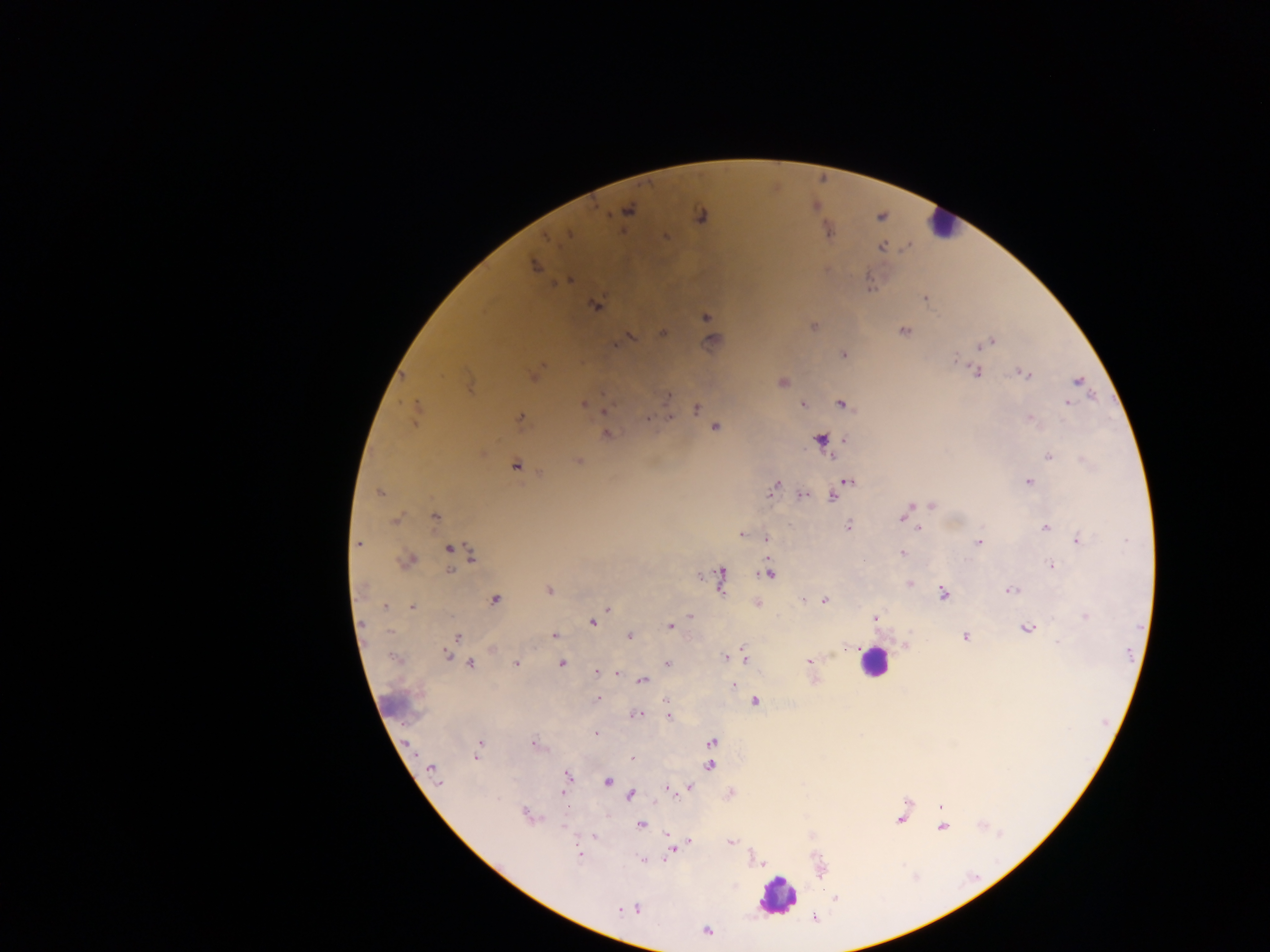

capture: mobile-phone photograph through a microscope
field_of_view: single
country: Ghana
leukocyte_locations: 'approximate centers as (x, y) in pixels: (873, 662), (778, 897)'
preparation: thick blood smear
image_size: 1270×952 pixels
plasmodium_parasite_locations: 'approximate centers as (x, y) in pixels: (630, 210), (664, 237), (549, 240), (595, 306), (704, 316), (904, 331), (662, 332), (627, 337), (992, 339), (619, 340), (712, 341), (844, 356), (954, 358), (977, 371), (1024, 373), (470, 382), (1077, 382), (783, 383), (669, 395), (418, 402), (839, 402), (582, 403), (803, 404), (1068, 404), (695, 409), (416, 412), (671, 415), (648, 417), (1028, 417), (519, 418), (715, 426), (607, 432), (1049, 456), (578, 462), (516, 466), (847, 481), (1028, 482), (777, 484), (379, 492), (771, 492), (801, 495), (832, 496), (931, 504), (910, 505), (433, 517), (392, 519), (900, 519), (849, 525), (919, 528), (1044, 528), (740, 535), (766, 538), (1076, 540), (979, 543), (360, 544), (449, 550), (901, 552), (471, 554), (1051, 565), (449, 568), (721, 572), (769, 575), (362, 587), (721, 587), (549, 591), (1009, 591), (943, 593), (495, 599), (823, 600), (757, 603), (384, 606), (413, 606), (607, 608), (689, 615), (1085, 615), (877, 618), (363, 622), (594, 624), (670, 626), (1027, 628), (630, 636), (457, 637), (555, 637), (963, 637), (1057, 641), (743, 646), (452, 650), (832, 653), (448, 655), (723, 656), (745, 659), (808, 661), (471, 662), (516, 662), (562, 662), (667, 662), (810, 668), (617, 671), (596, 672), (610, 673), (620, 674), (814, 678), (641, 680), (733, 685), (597, 698), (662, 700), (755, 702), (635, 714), (669, 718), (596, 733), (711, 741), (407, 743), (536, 743), (480, 744), (631, 759), (710, 765), (432, 769), (567, 775), (435, 779), (608, 782), (440, 784), (691, 788), (667, 790), (684, 790), (563, 794), (673, 794), (631, 795), (940, 807), (525, 814), (899, 820), (640, 823), (567, 831), (666, 833), (594, 837), (688, 842), (730, 842), (671, 851), (579, 853), (641, 861), (836, 900), (706, 930)'